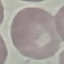
result = negative for malaria parasites
preparation = thin blood film
capture = smartphone through the microscope eyepiece
image type = cell patch, automatically extracted from a larger field of view and resized to 64 × 64 pixels
stain = Giemsa